Assess this cell for malaria.
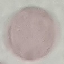

It is uninfected.

Summary:
  - Image type: automatically extracted cell patch, resized to 64 × 64 pixels
  - Preparation: thin blood film
  - Capture: smartphone through the microscope eyepiece
  - Stain: Giemsa